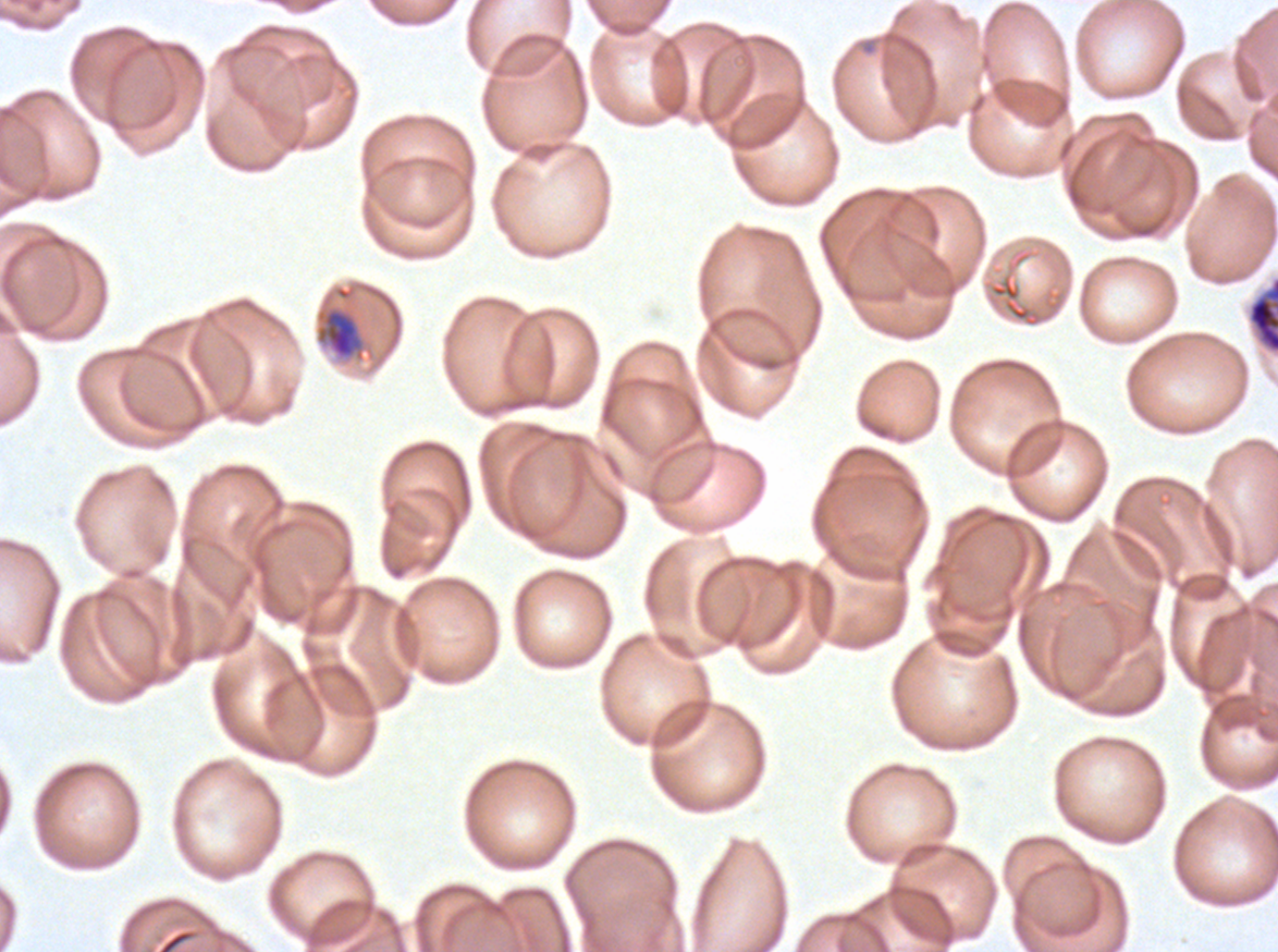

notation = approximate bounding boxes as [x1, y1, x2, y2] in pixels
late-ring/early-trophozoite locations = [314, 306, 365, 362]
early schizont locations = [1247, 276, 1277, 353]
stain = Giemsa
life-cycle stages observed = late-ring/early-trophozoite, early schizont
specimen = Plasmodium falciparum from a patient in The Gambia, cultured ex vivo for 24 to 48 hours
image size = 1278×952 pixels
field of view = one sub-image of a larger composite
preparation = thin blood smear